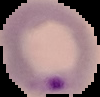

preparation = thin blood film
image size = 100×97 pixels
result = malaria parasites identified
image type = segmented cell region on a black background